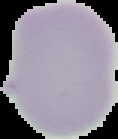 Cell region segmented out of the field of view; the surrounding area is masked to black. From a thin blood film. Image is 118×139 pixels. Malaria status: uninfected.